Locate every malaria parasite.
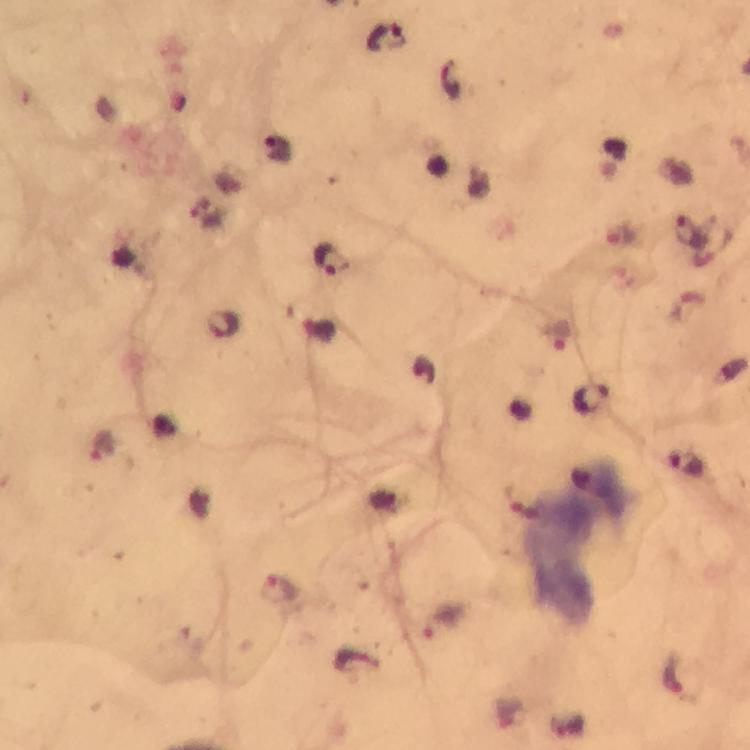
Approximate centers as {x, y} in pixels.
Malaria parasites: {388, 38}, {276, 147}, {691, 232}, {332, 259}, {224, 325}, {557, 338}, {595, 399}, {106, 447}, {686, 465}, {523, 504}, {281, 591}, {443, 623}, {675, 676}.

cropped from = a single field of view
immersion oil = used
magnification = 100x
context = from a malaria diagnostic workup
capture = smartphone camera through the microscope
stain = Giemsa
preparation = thick blood film
image size = 750×750 pixels